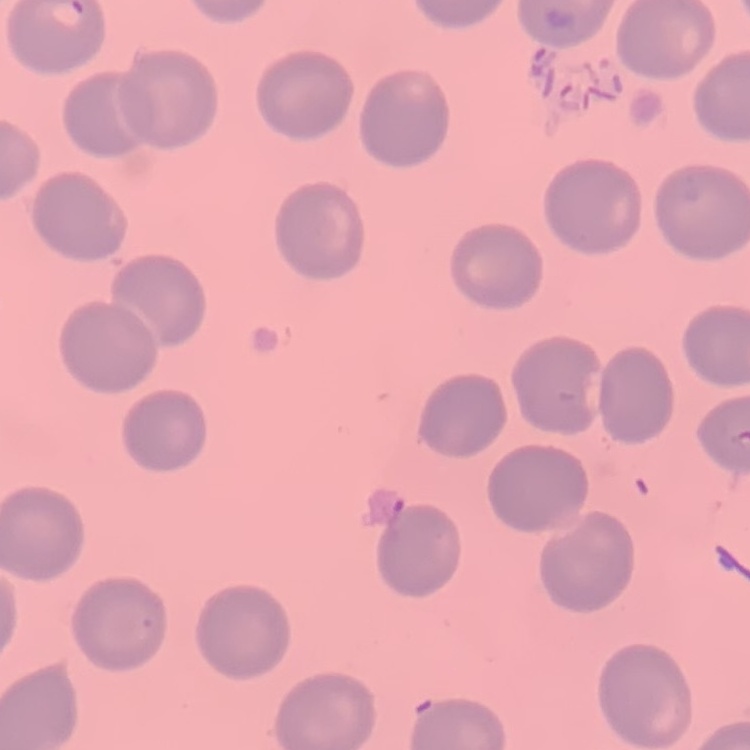

Summary:
  - Red blood cell morphology: no rouleaux formation
  - Stain: Field's or Giemsa
  - Preparation: thin peripheral smear
  - Image type: one tile cut from a larger photomicrograph